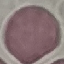

malaria_status: uninfected
preparation: thin blood film
stain: Giemsa
capture: smartphone through the microscope eyepiece
image_type: automatically extracted cell patch, resized to 64 × 64 pixels